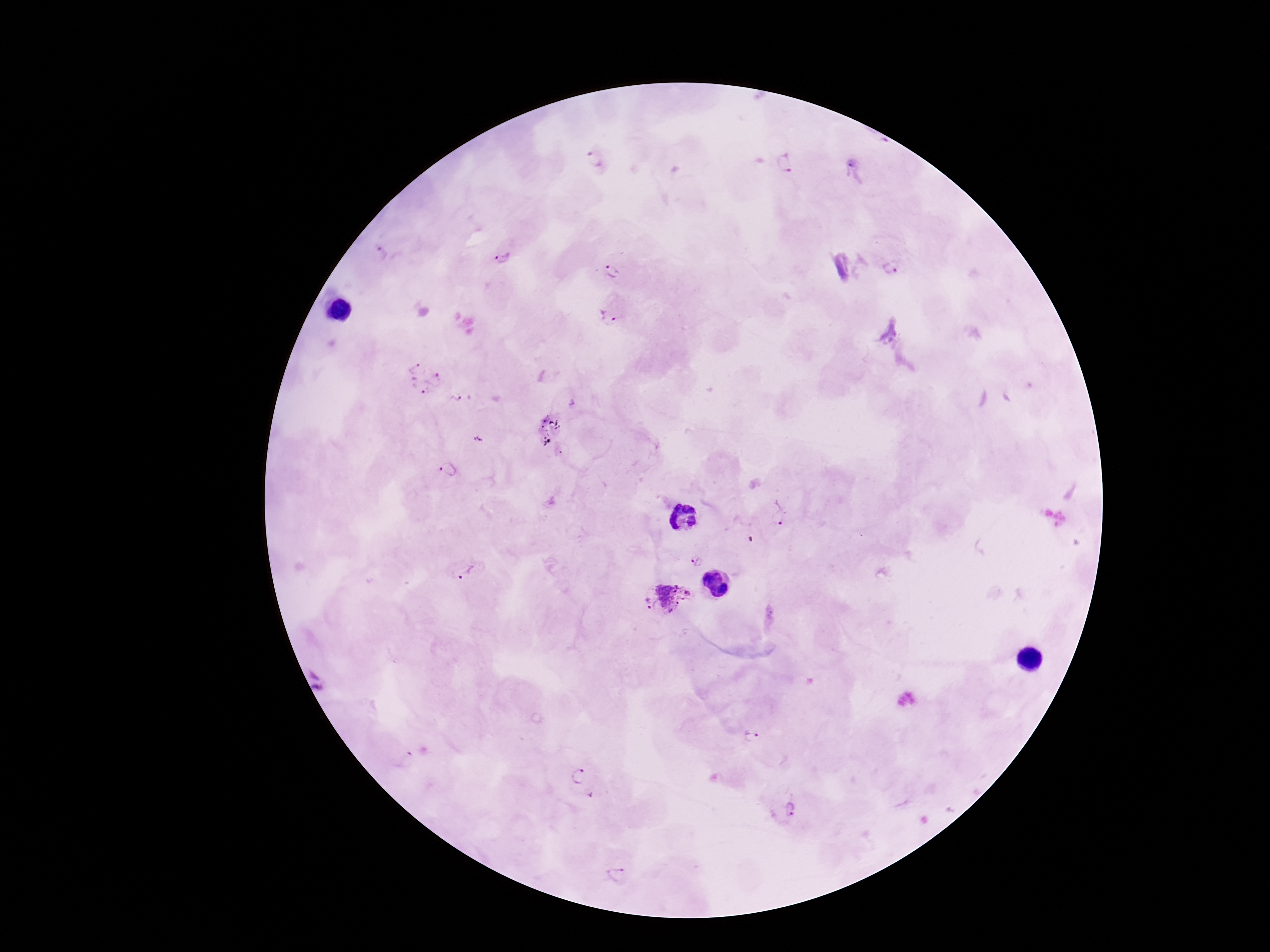
Plasmodium parasite locations = approximate centers as {x, y} in pixels: {593, 156}, {786, 162}, {380, 256}, {502, 258}, {891, 266}, {611, 272}, {608, 316}, {424, 377}, {462, 399}, {479, 440}, {449, 470}, {779, 512}, {697, 561}, {464, 572}, {666, 599}, {320, 678}, {751, 735}, {404, 759}, {579, 778}, {790, 809}, {615, 876}
stain = Giemsa
capture = smartphone camera through the microscope eyepiece
field of view = one from this slide
preparation = thick peripheral-blood smear
image size = 1270×952 pixels
patient malaria status = positive
magnification = 100x